Draw a bounding box around every leukocyte (white blood cell).
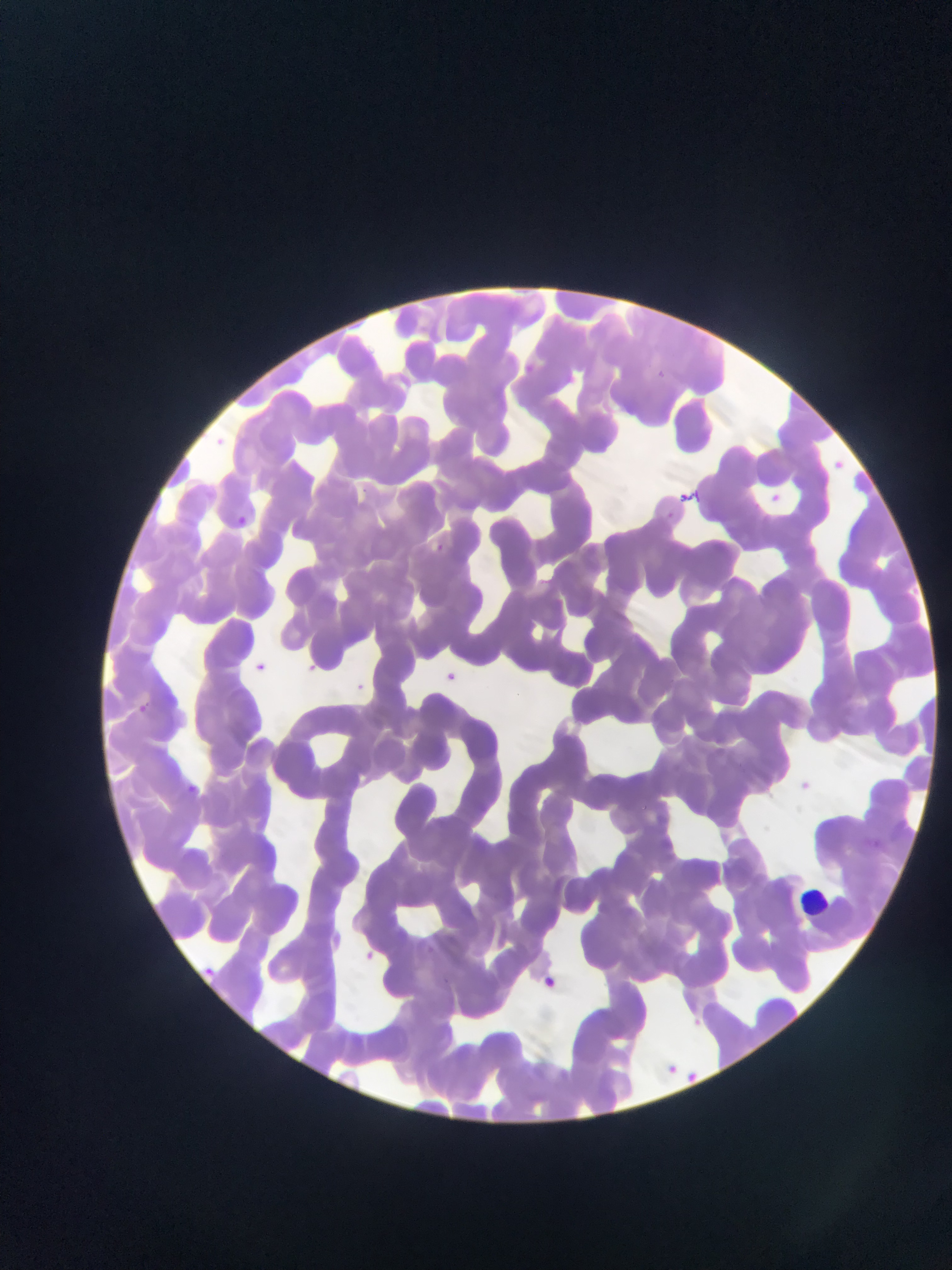

Approximate bounding boxes as (left, top, right, bottom) in pixels.
Leukocytes: (800, 889, 838, 922).

country = Ghana
field of view = single
malaria parasite locations = approximate bounding boxes as (left, top, right, bottom) in pixels: (655, 364, 670, 381), (831, 455, 845, 470), (682, 487, 707, 509), (767, 488, 787, 508), (663, 505, 686, 526), (238, 515, 255, 529), (428, 542, 445, 555), (252, 661, 265, 670), (309, 662, 325, 683), (446, 667, 460, 677), (358, 680, 364, 693), (135, 700, 151, 715), (801, 778, 816, 795), (185, 780, 202, 794), (415, 940, 437, 955), (363, 949, 385, 964), (203, 964, 228, 982), (541, 970, 555, 990), (691, 1010, 708, 1030), (666, 1060, 680, 1076), (684, 1068, 705, 1091)
preparation = thin blood film
capture = mobile-phone photograph through a microscope
image size = 952×1270 pixels